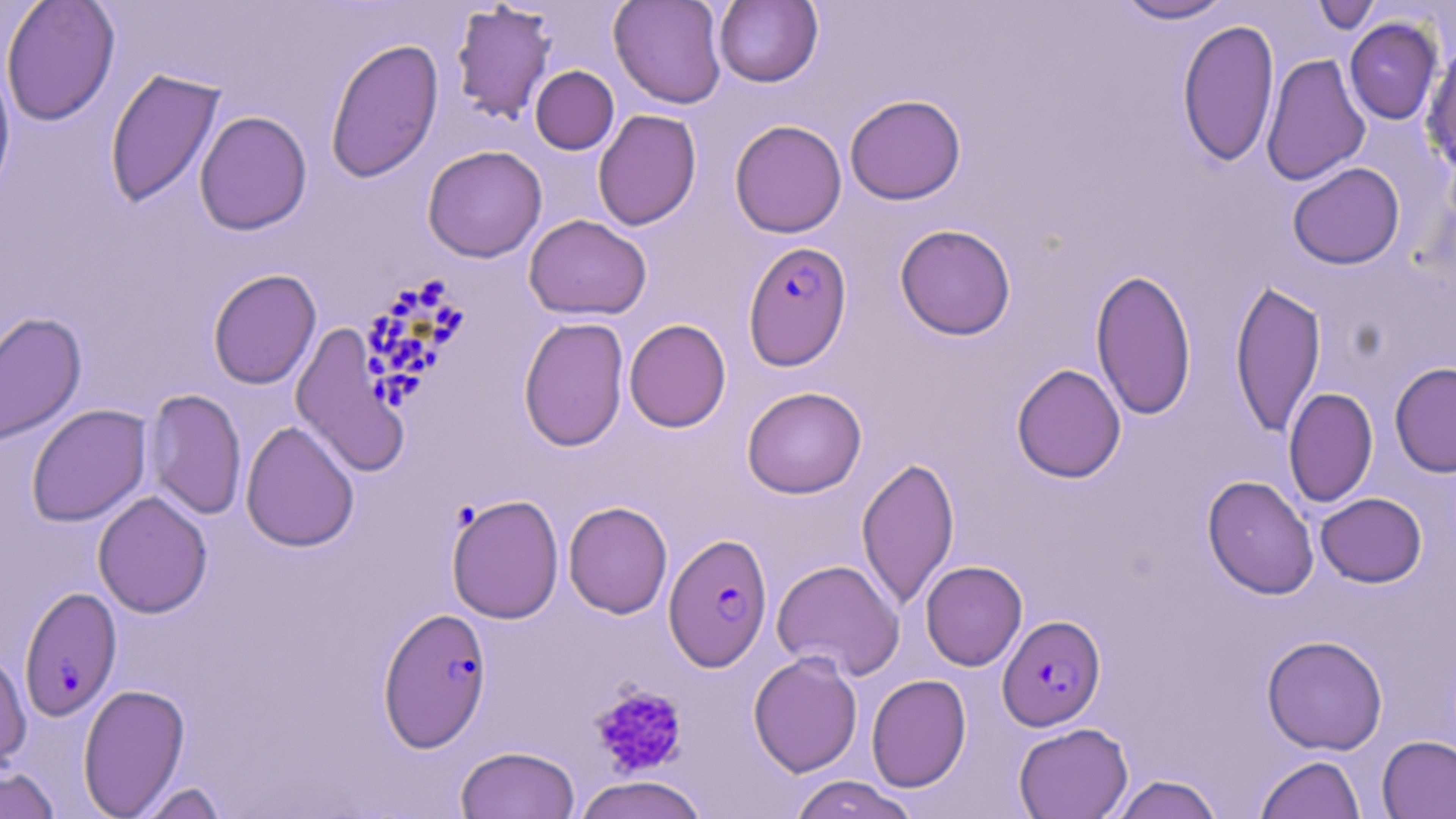

Summary:
  - Coordinate format: approximate bounding boxes as (x1,y1)-(x2,y2) corner pairs in pixels
  - Uninfected red blood cell locations: (1,0)-(120,126), (609,0)-(727,109), (713,0)-(823,88), (1114,0)-(1233,24), (1310,0)-(1382,33), (450,2)-(558,124), (1177,18)-(1279,167), (1344,18)-(1442,124), (324,37)-(445,184), (1422,43)-(1456,177), (1261,53)-(1371,187), (0,61)-(16,202), (530,66)-(619,154), (104,67)-(226,209), (845,94)-(966,205), (592,109)-(702,231), (194,110)-(312,235), (730,119)-(847,238), (422,145)-(547,262), (1287,162)-(1405,269), (524,214)-(652,321), (894,224)-(1016,340), (1090,267)-(1197,421), (207,268)-(322,390), (1230,278)-(1327,439), (0,310)-(87,448), (518,317)-(629,452), (624,318)-(731,433), (290,324)-(409,479), (1390,362)-(1456,477), (1011,363)-(1126,483), (742,386)-(867,499), (1283,387)-(1378,508), (143,388)-(247,520), (26,404)-(152,527), (240,420)-(360,552), (856,455)-(959,611), (1202,475)-(1319,599), (92,490)-(213,618), (1315,492)-(1427,587), (446,494)-(565,623), (563,501)-(672,619), (771,558)-(905,680), (920,560)-(1027,671), (1262,634)-(1388,755), (0,647)-(32,773), (748,651)-(862,777), (866,674)-(971,792), (77,683)-(190,818), (1013,722)-(1133,819), (1377,735)-(1456,818), (455,745)-(580,818), (1255,755)-(1366,819), (0,765)-(61,819), (1109,774)-(1224,819), (573,775)-(708,819), (787,775)-(919,819), (134,781)-(229,818)
  - Plasmodium falciparum-infected red blood cell locations: (742,240)-(853,372), (365,278)-(472,418), (664,532)-(772,671), (18,586)-(122,722), (377,606)-(492,752), (998,614)-(1105,731)
  - Platelet locations: (589,684)-(689,779)
  - Slide-level diagnosis: Plasmodium falciparum
  - Magnification: 1000x
  - Preparation: thin blood smear
  - Image size: 1456×819 pixels
  - Modality: optical microscopy
  - Field of view: one of a larger specimen
  - Stain: May-Grünwald-Giemsa